Assess this cell for malaria.
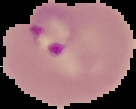

Parasitized.

Summary:
  - Image size: 136×109 pixels
  - Preparation: thin blood smear
  - Image type: segmented cell region with the area outside set to black